Locate every leukocyte (white blood cell).
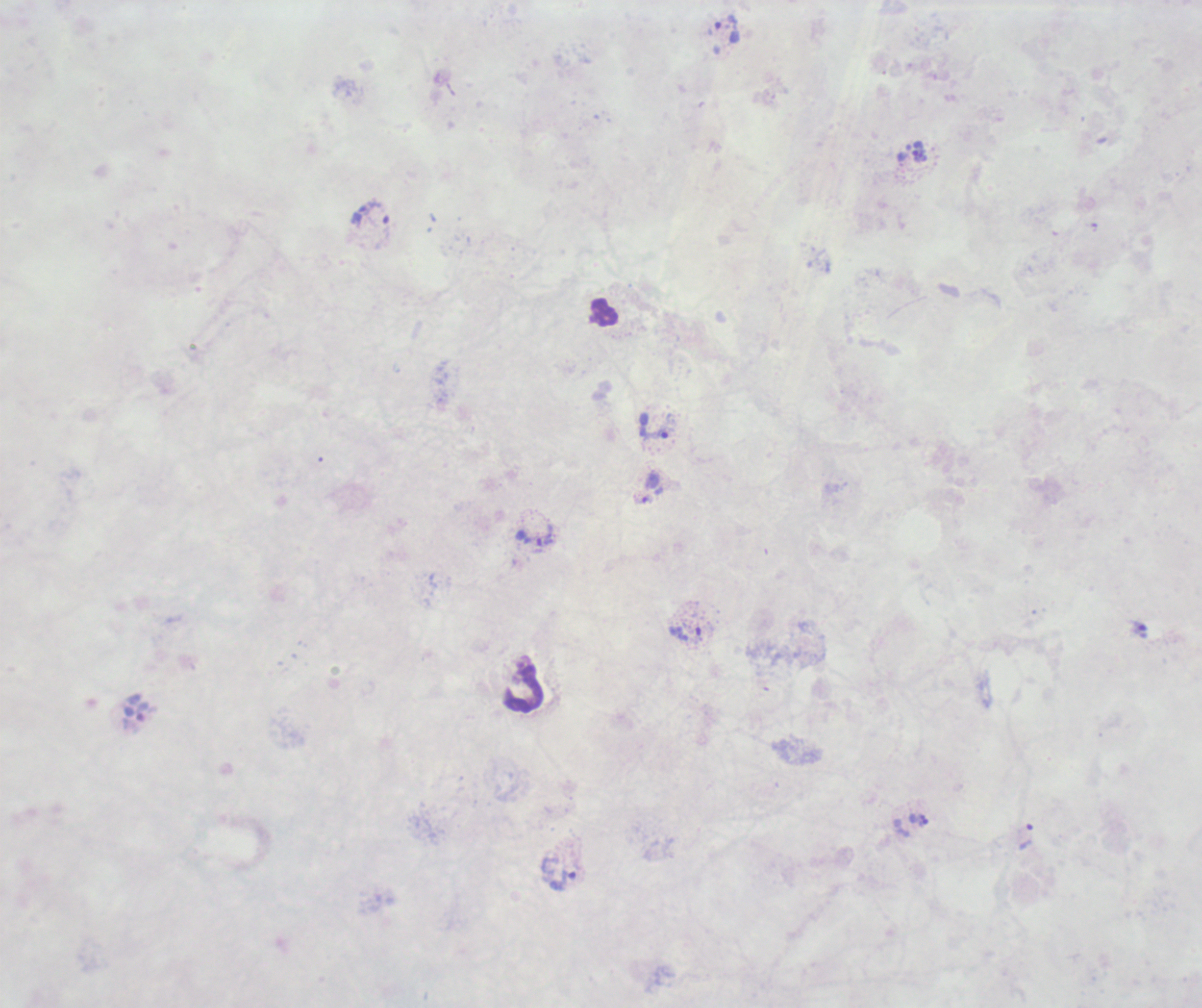
Approximate centers as (x, y) in pixels.
Leukocytes: (603, 313), (523, 689).

coordinate format = approximate centers as (x, y) in pixels
trophozoite locations = (726, 30), (911, 152), (371, 213), (653, 425), (643, 500), (535, 536), (685, 632), (1026, 835), (564, 880)
result = Plasmodium parasites detected
context = previously used in a real diagnosis
field of view = single
background quality = poor
coloration quality = bad
preparation = thick blood smear
image size = 1202×1008 pixels
magnification = 100x
stain = Romanowsky